Classify this cell by malaria status.
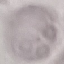
Uninfected.

Summary:
  - Capture: smartphone through the microscope eyepiece
  - Stain: Giemsa
  - Image type: automatically extracted cell patch, resized to 64 × 64 pixels
  - Preparation: thin blood film